Assess this cell for malaria.
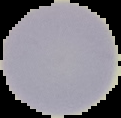
Uninfected.

preparation = thin blood smear
image size = 121×118 pixels
image type = cell region segmented out of the field of view; surrounding area masked to black